State which parasite is depicted.
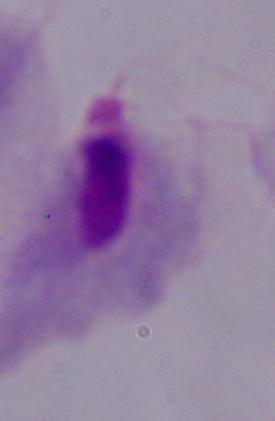
A trichomonad.

Captured at 1000x magnification. Photomicrograph.